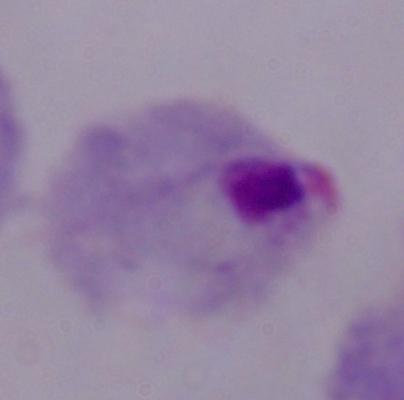
identification = trichomonad
magnification = 1000x
modality = micrograph